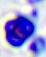
identification: white blood cell
magnification: 400x
modality: photomicrograph